Report the malaria status of this cell.
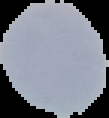
It is uninfected.

image size = 109×118 pixels
image type = segmented cell region with the area outside set to black
preparation = thin blood smear